Classify this cell by malaria status.
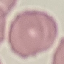

It is uninfected.

Summary:
  - Stain: Giemsa
  - Image type: cell patch, automatically extracted from a larger field of view and resized to 64 × 64 pixels
  - Preparation: thin smear
  - Capture: smartphone camera at the microscope eyepiece